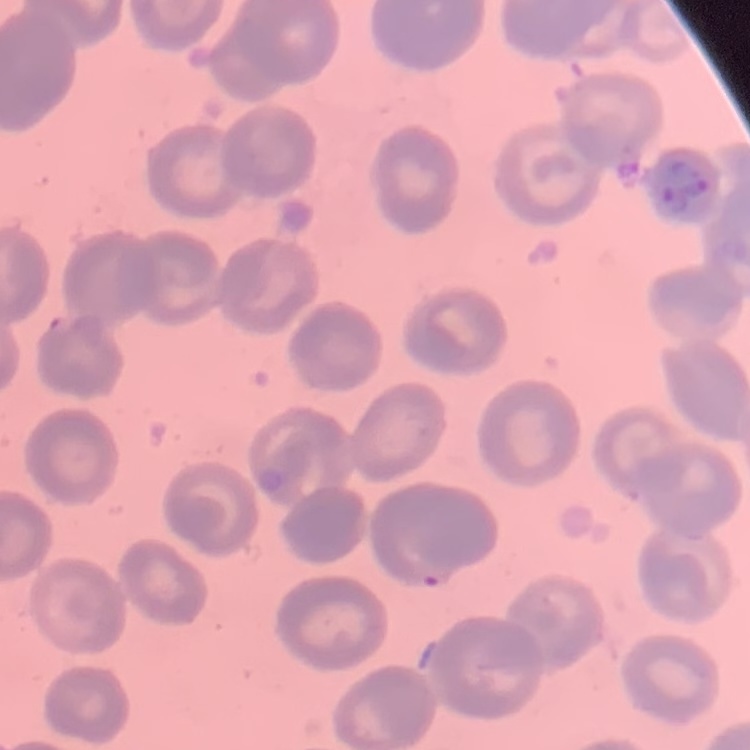
The erythrocytes exhibit no rouleaux formation. Square crop of a larger photomicrograph. Field's or Giemsa stain. Thin peripheral smear.